Describe the morphology of the red blood cells.
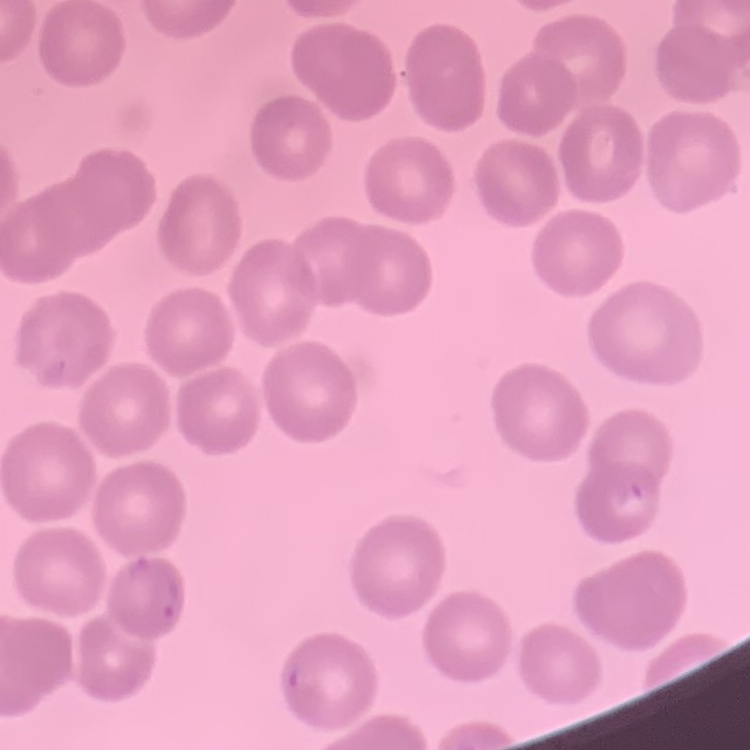
No rouleaux formation.

Field's or Giemsa stain. Thin blood smear. Square crop of a larger photomicrograph.